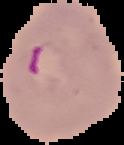

preparation: thin blood smear
image_type: segmented cell region on a black background
malaria_status: parasitized
image_size: 124×145 pixels